Assess the morphology of the erythrocytes.
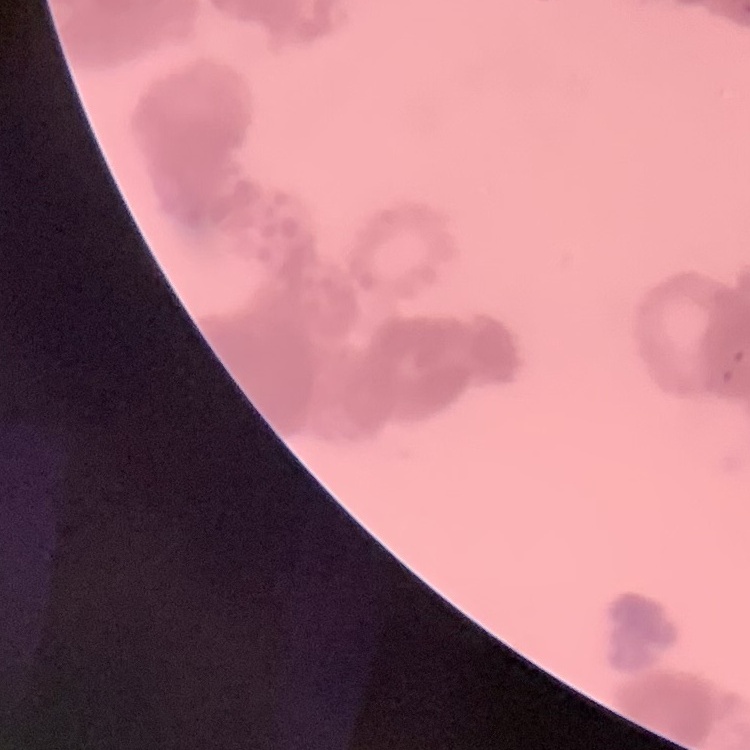

They show rouleaux formation.

Field's or Giemsa stain. One tile cut from a larger photomicrograph. Thin peripheral smear.